Assess the morphology of the red blood cells.
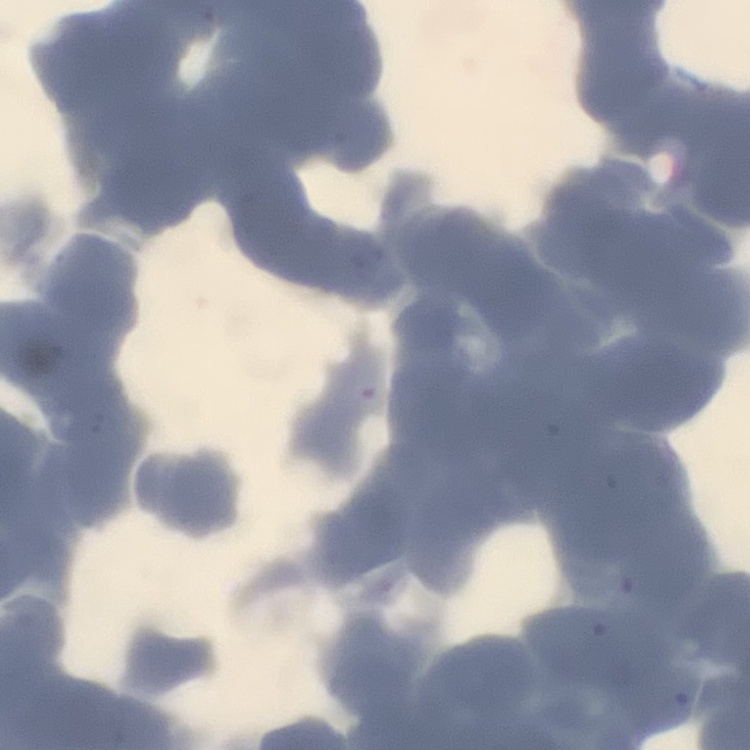

Rouleaux formation.

image type = square crop of a larger photomicrograph
stain = Field's or Giemsa
preparation = thin blood smear